Locate every Plasmodium parasite.
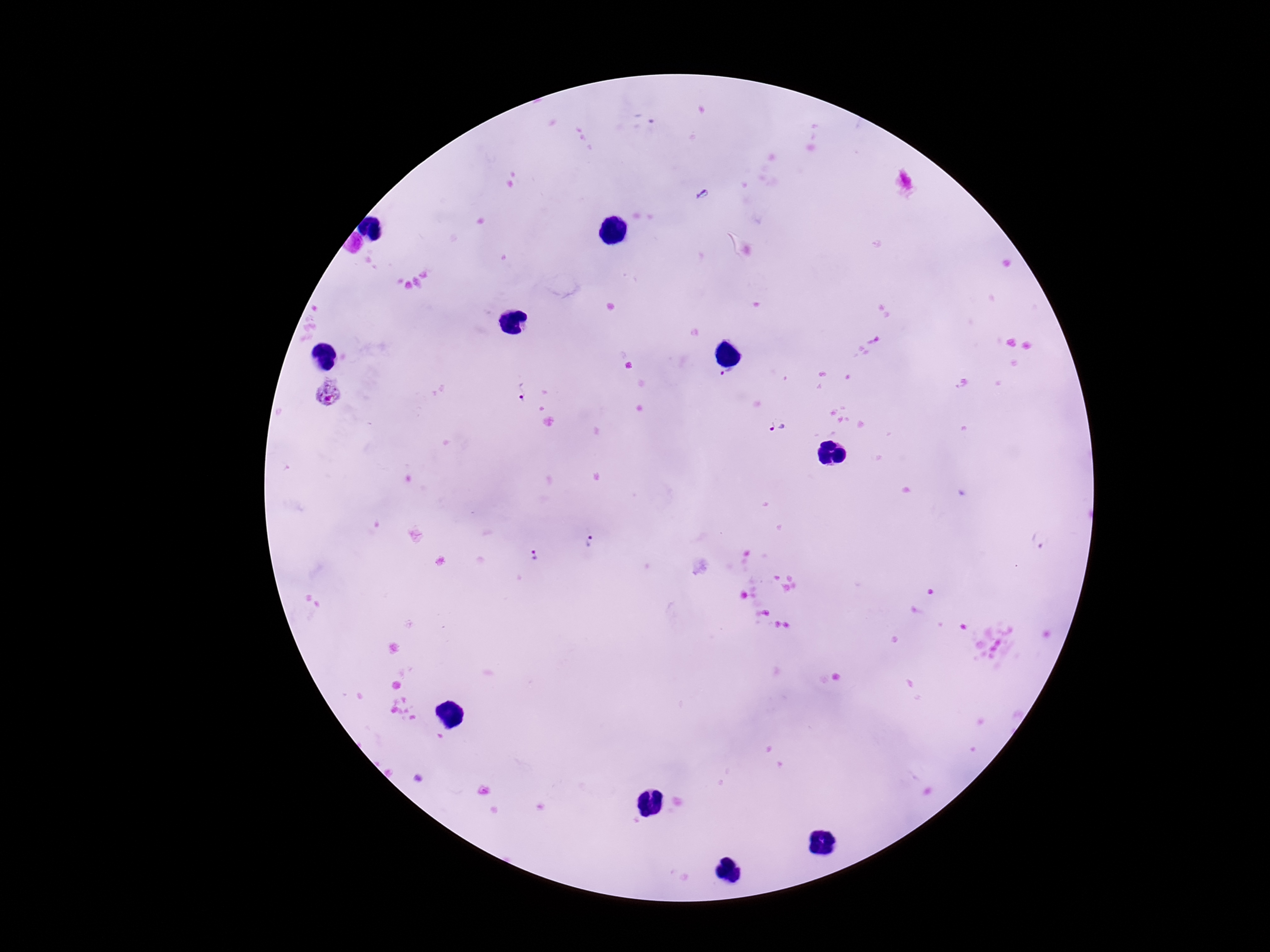

Approximate centers as {x, y} in pixels.
Plasmodium parasites: {729, 377}, {521, 391}, {329, 395}, {779, 426}, {589, 541}, {1041, 541}, {535, 554}.

patient malaria status = positive
stain = Giemsa
field of view = single
image size = 1270×952 pixels
capture = smartphone camera through the microscope eyepiece
magnification = 100x
preparation = thick blood film